Identify the parasite.
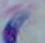

This is Toxoplasma gondii.

magnification = 1000x
modality = micrograph